Classify this cell by malaria status.
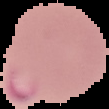
Parasitized.

image size = 109×109 pixels
image type = segmented cell region on a black background
preparation = thin blood smear